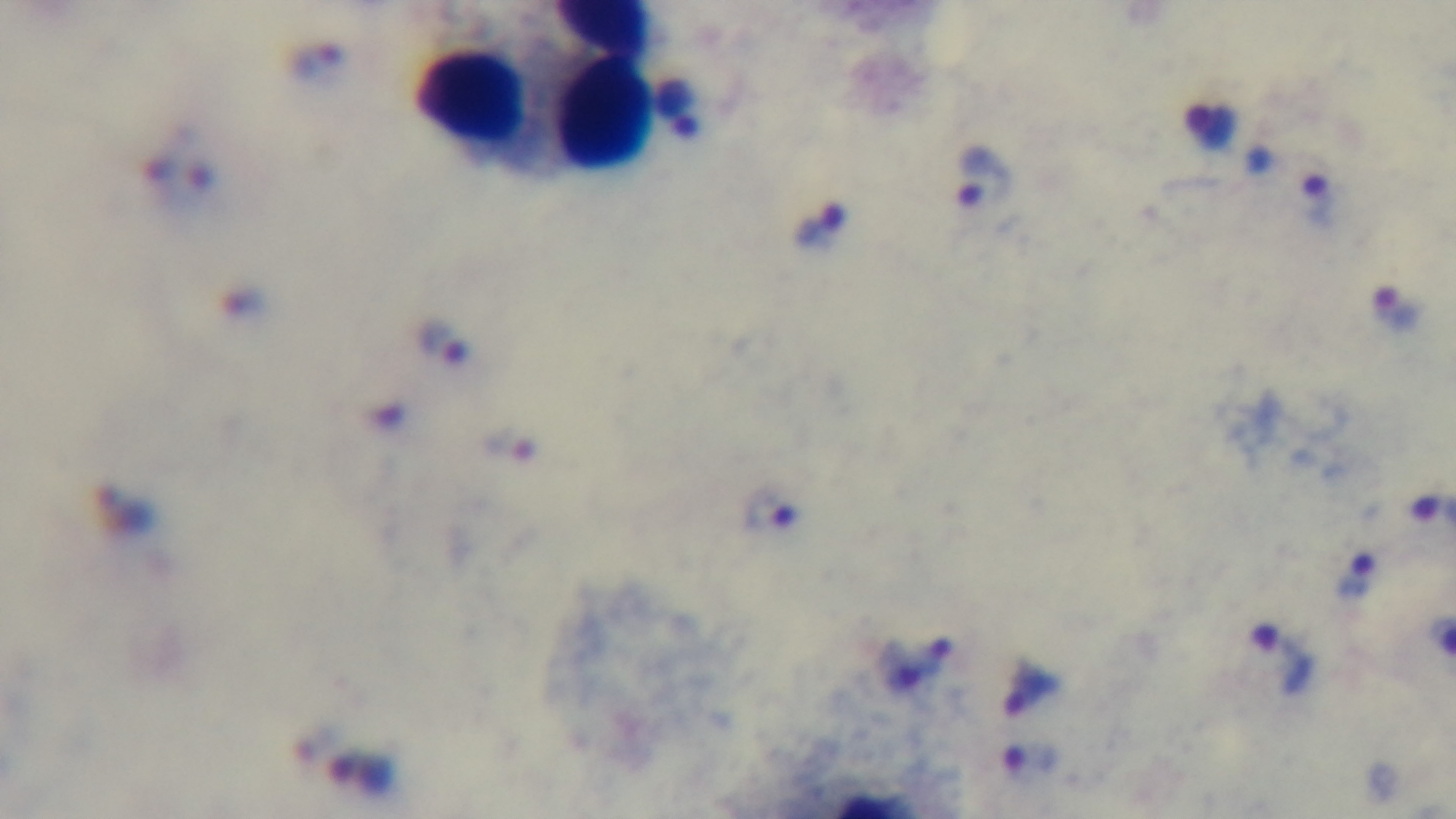
Summary:
  - Stain: Giemsa
  - Preparation: thick
  - Objective: 100x oil immersion
  - Modality: light microscopy
  - Capture: mounted 4K digital camera
  - Malaria status: positive
  - Field of view: one from the slide